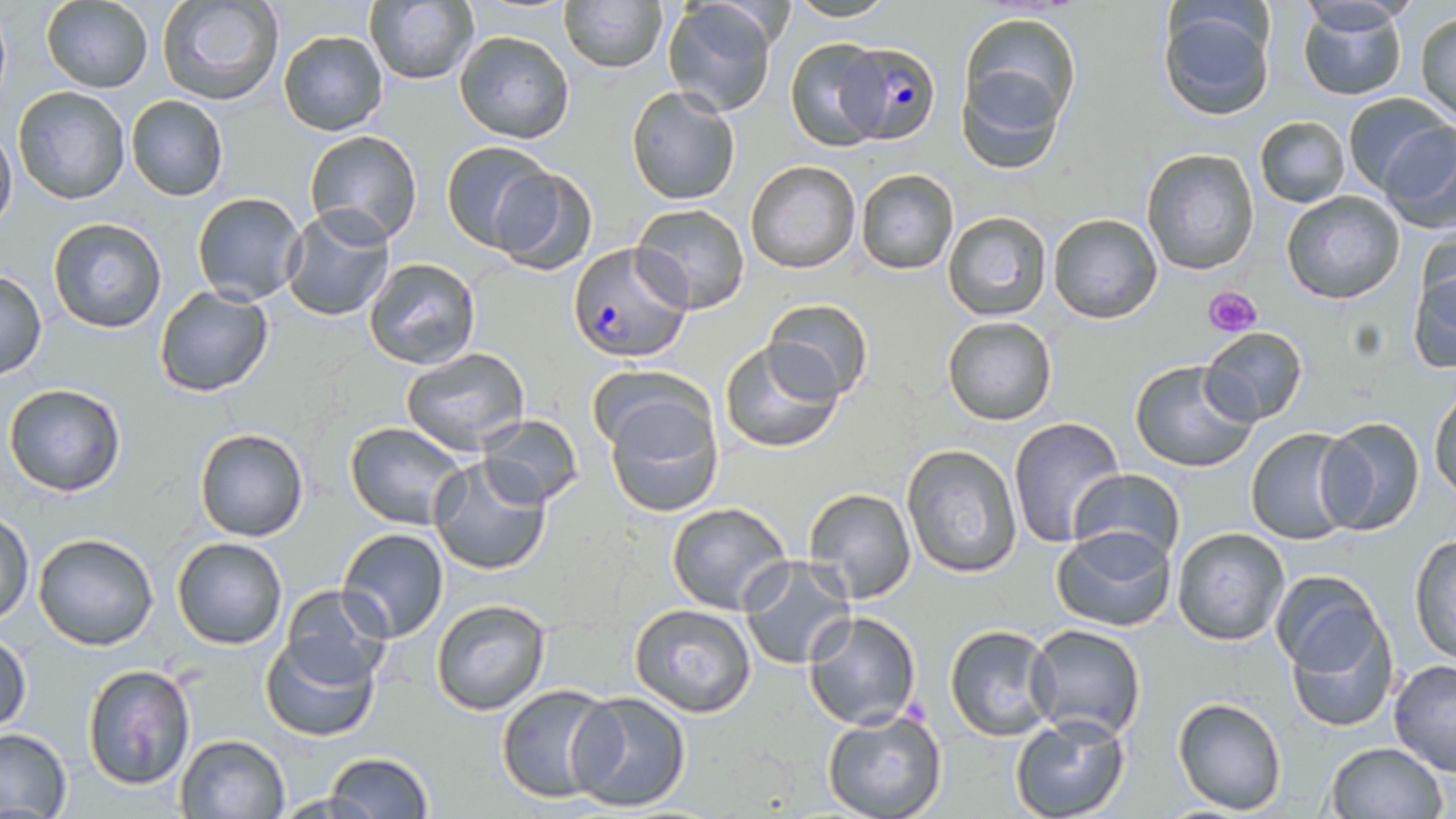
{
  "slide_level_diagnosis": "Plasmodium falciparum",
  "image_size": "1456×819 pixels",
  "plasmodium_falciparum_infected_red_blood_cell_locations": "approximate bounding boxes as [x1, y1, x2, y2] in pixels: [837, 42, 940, 144], [568, 242, 691, 362]",
  "uninfected_red_blood_cell_locations": "approximate bounding boxes as [x1, y1, x2, y2] in pixels: [156, 0, 286, 108], [558, 0, 667, 72], [41, 1, 153, 92], [663, 1, 777, 116], [783, 1, 905, 23], [1297, 1, 1410, 102], [364, 2, 479, 85], [1156, 2, 1277, 120], [960, 11, 1082, 128], [1415, 11, 1456, 123], [277, 30, 388, 136], [454, 30, 575, 144], [785, 38, 887, 151], [957, 63, 1069, 175], [11, 86, 130, 205], [626, 86, 739, 205], [1341, 91, 1452, 198], [124, 95, 229, 202], [1254, 115, 1351, 208], [1376, 122, 1456, 234], [0, 123, 16, 233], [304, 129, 424, 247], [442, 141, 555, 250], [1140, 147, 1261, 275], [746, 160, 860, 274], [487, 165, 597, 276], [854, 168, 960, 276], [1280, 191, 1406, 306], [191, 192, 307, 306], [629, 202, 751, 314], [281, 206, 396, 323], [943, 211, 1051, 320], [1048, 213, 1162, 324], [46, 216, 168, 335], [1412, 232, 1455, 331], [364, 257, 481, 371], [1406, 263, 1456, 375], [0, 269, 47, 378], [153, 285, 274, 398], [763, 298, 874, 402], [941, 316, 1058, 425], [1199, 326, 1309, 427], [719, 337, 844, 453], [401, 346, 530, 456], [1129, 359, 1260, 473], [589, 365, 711, 460], [3, 382, 127, 497], [1430, 387, 1455, 505], [603, 390, 724, 518], [476, 415, 584, 509], [1314, 416, 1427, 535], [1007, 417, 1127, 546], [343, 421, 471, 530], [1246, 427, 1360, 546], [192, 428, 309, 542], [900, 443, 1022, 578], [429, 456, 552, 576], [1068, 469, 1186, 564], [801, 488, 920, 606], [665, 501, 795, 616], [0, 513, 34, 624], [338, 527, 449, 642], [1051, 527, 1177, 634], [1172, 527, 1289, 645], [33, 533, 158, 651], [1410, 533, 1455, 667], [171, 537, 288, 651], [737, 555, 856, 671], [1268, 569, 1387, 687], [276, 584, 394, 689], [430, 598, 553, 716], [1283, 599, 1397, 735], [628, 602, 759, 719], [802, 610, 922, 730], [944, 624, 1059, 742], [1025, 625, 1147, 741], [260, 629, 382, 743], [0, 632, 33, 735], [1388, 657, 1456, 775], [81, 664, 194, 793], [496, 684, 619, 804], [567, 691, 692, 813], [1172, 696, 1287, 815], [823, 708, 946, 819], [1009, 711, 1130, 819], [1, 729, 71, 817], [174, 734, 291, 819], [1324, 741, 1447, 819], [324, 752, 433, 819]",
  "stain": "May-Grünwald-Giemsa",
  "platelet_locations": "approximate bounding boxes as [x1, y1, x2, y2] in pixels: [1203, 284, 1261, 337]",
  "modality": "optical microscopy",
  "preparation": "thin blood smear",
  "field_of_view": "single",
  "magnification": "1000x"
}